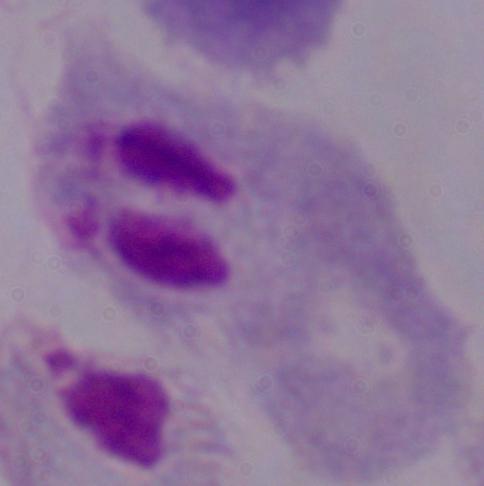
Micrograph. A trichomonad is seen. 1000x magnification.